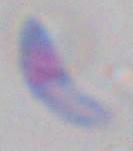 1000x magnification. Photomicrograph. Toxoplasma gondii is seen.